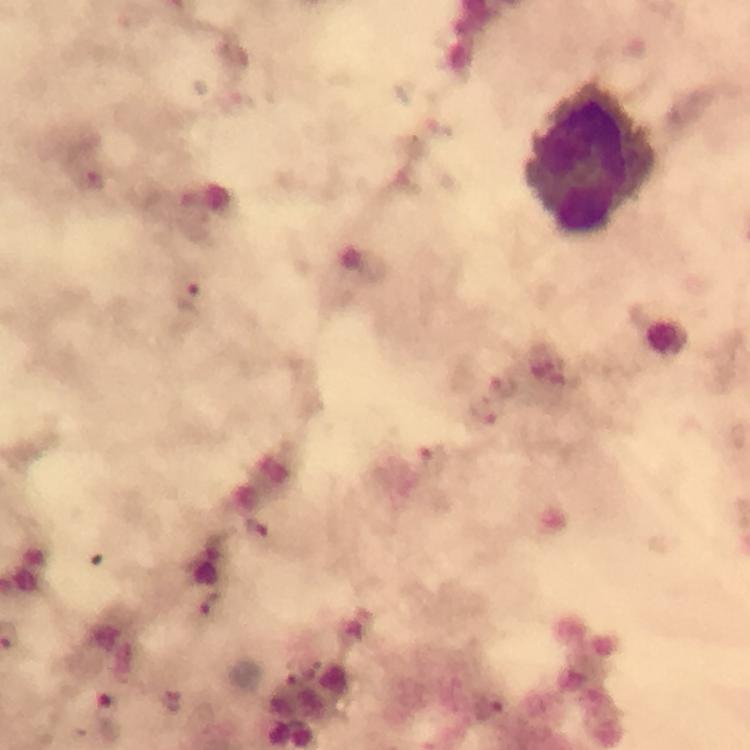

Approximate centers as [x, y] in pixels.
Summary:
  - Leukocyte locations: [592, 156]
  - Plasmodium parasite locations: [94, 179], [189, 295], [504, 386], [487, 411], [435, 462], [255, 530], [209, 605]
  - Capture: smartphone mounted on the microscope
  - Stain: Giemsa
  - Magnification: 100x
  - Image size: 750×750 pixels
  - Cropped from: a single field of view
  - Immersion oil: used
  - Preparation: thick blood film
  - Context: from a diagnostic examination for malaria